Give the extent of all uninfected red blood cells.
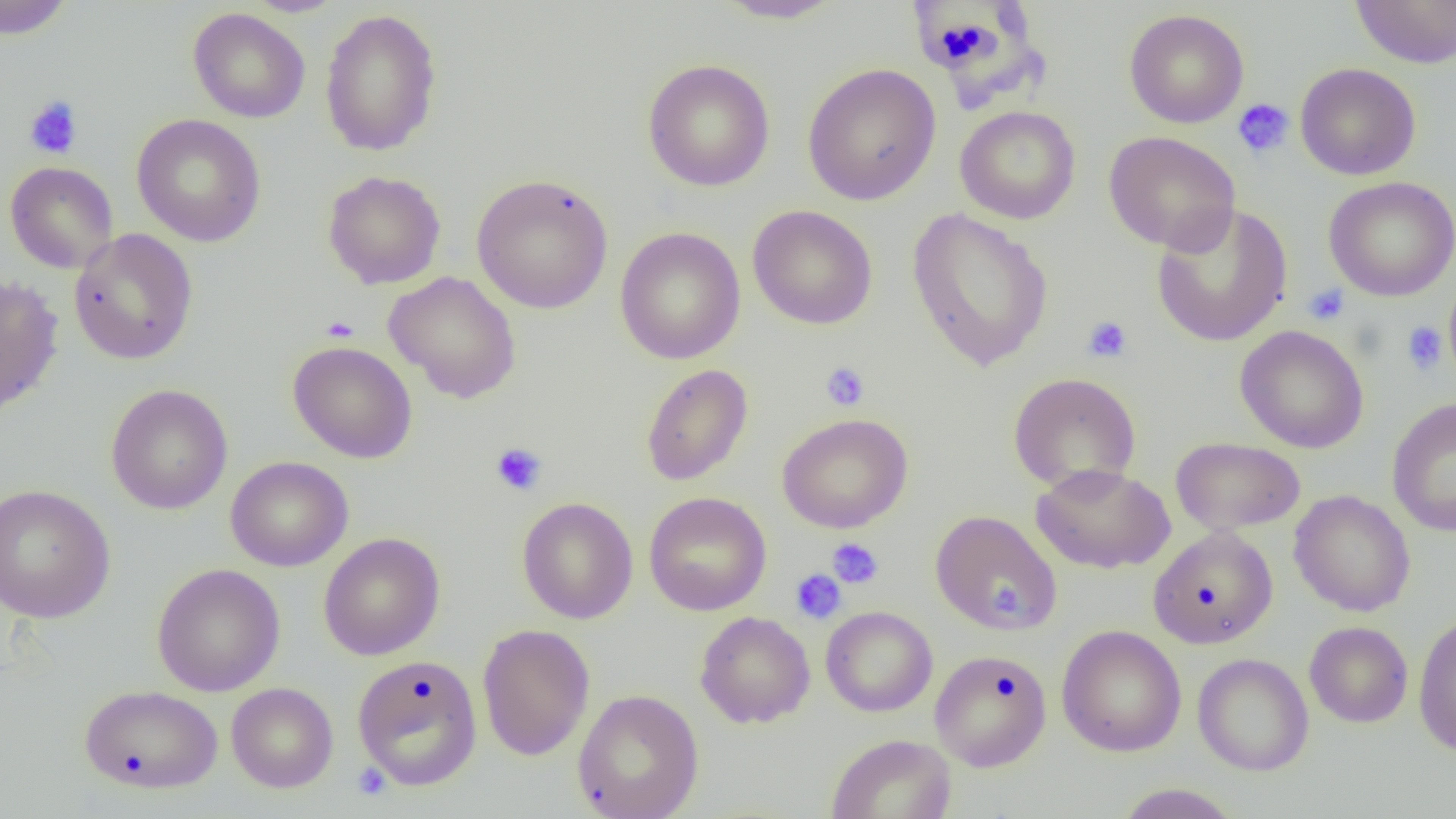
Approximate bounding boxes as (x1,y1)-(x2,y2) corner pairs in pixels.
Uninfected red blood cells: (0,0)-(75,40), (714,0)-(847,24), (1351,0)-(1456,68), (188,8)-(310,123), (320,8)-(442,156), (1124,9)-(1249,128), (642,58)-(775,192), (1295,62)-(1421,180), (802,63)-(941,205), (955,105)-(1081,224), (131,113)-(267,247), (1103,131)-(1240,254), (5,161)-(119,274), (322,170)-(446,289), (471,173)-(614,315), (1323,176)-(1456,302), (1150,203)-(1293,348), (747,204)-(878,330), (906,207)-(1054,371), (615,226)-(745,364), (69,228)-(198,365), (383,271)-(522,404), (0,275)-(64,418), (1443,282)-(1456,383), (1234,325)-(1369,454), (288,341)-(418,463), (641,363)-(753,486), (1007,372)-(1142,492), (105,384)-(233,515), (1387,397)-(1456,538), (776,413)-(913,533), (1170,436)-(1306,536), (225,456)-(353,572), (1031,463)-(1175,574), (0,483)-(115,623), (1289,490)-(1416,616), (644,491)-(771,616), (517,497)-(638,624), (931,510)-(1062,634), (1147,526)-(1279,648), (319,532)-(445,660), (151,563)-(286,696), (820,605)-(938,717), (695,611)-(815,728), (1413,613)-(1456,755), (1304,621)-(1413,727), (477,624)-(595,761), (1056,624)-(1187,756), (929,649)-(1052,771), (1192,653)-(1314,776), (352,654)-(483,790), (226,682)-(338,793), (78,684)-(223,794), (573,688)-(704,819), (826,733)-(957,819), (1113,783)-(1243,819).

slide-level diagnosis = negative for blood parasites
platelet locations = approximate bounding boxes as (x1,y1)-(x2,y2) corner pairs in pixels: (24,95)-(83,159), (1232,98)-(1294,159), (1303,284)-(1349,325), (320,315)-(360,342), (1082,315)-(1133,363), (1402,321)-(1448,375), (820,361)-(871,412), (490,442)-(547,496), (827,538)-(884,589), (790,569)-(847,625), (991,585)-(1030,624), (352,762)-(392,801)
field of view = one of a larger specimen
image size = 1456×819 pixels
preparation = thin blood smear
modality = light microscopy
magnification = 1000x